Assess this cell for malaria.
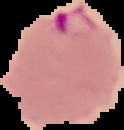
Parasitized.

image size = 124×130 pixels
image type = segmented cell region on a black background
preparation = thin blood film